Give the location of every WBC.
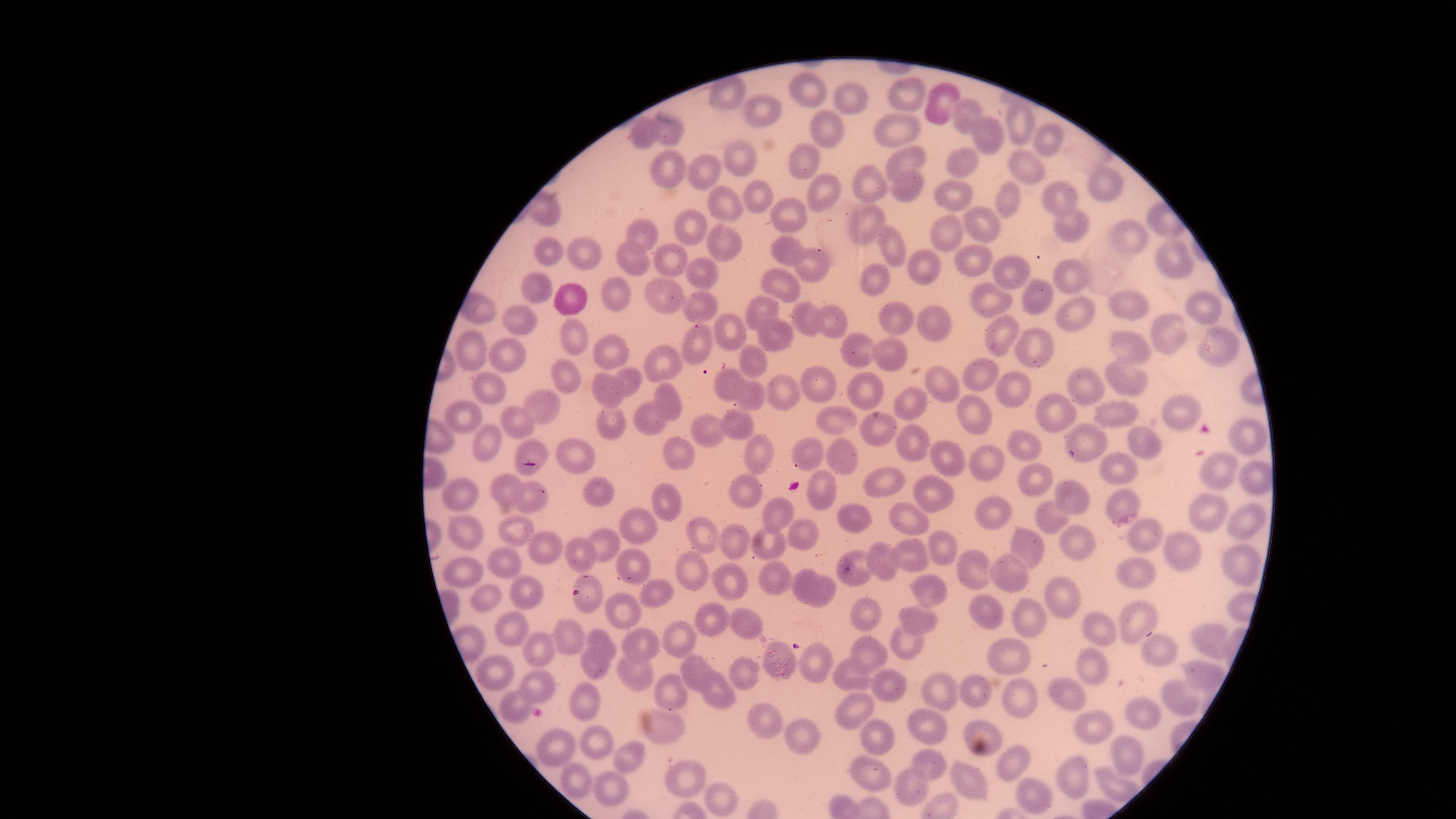
No WBCs identified.

Approximate marker points as {x, y} in pixels.
Summary:
  - Uninfected RBCs: {811, 80}, {914, 95}, {846, 96}, {942, 103}, {761, 109}, {966, 114}, {1020, 126}, {645, 127}, {825, 128}, {899, 128}, {670, 131}, {989, 135}, {1050, 141}, {742, 156}, {962, 159}, {802, 162}, {667, 165}, {903, 166}, {1026, 166}, {701, 174}, {863, 183}, {1100, 183}, {823, 190}, {753, 191}, {901, 192}, {951, 192}, {1014, 201}, {1060, 201}, {721, 202}, {787, 211}, {868, 215}, {1070, 223}, {988, 224}, {693, 226}, {1127, 232}, {646, 234}, {951, 234}, {726, 245}, {787, 247}, {896, 248}, {546, 250}, {588, 254}, {970, 255}, {804, 256}, {674, 258}, {635, 259}, {1167, 261}, {926, 262}, {696, 266}, {1008, 271}, {785, 276}, {880, 278}, {1065, 279}, {1032, 288}, {619, 291}, {664, 293}, {535, 295}, {987, 300}, {567, 301}, {704, 304}, {1203, 305}, {759, 307}, {1119, 308}, {1070, 311}, {834, 315}, {523, 316}, {929, 318}, {810, 320}, {898, 320}, {727, 329}, {995, 331}, {572, 333}, {773, 336}, {691, 339}, {1174, 339}, {1032, 341}, {612, 345}, {1129, 346}, {476, 347}, {856, 349}, {1219, 350}, {511, 354}, {884, 356}, {753, 359}, {663, 362}, {627, 374}, {566, 376}, {983, 377}, {1129, 378}, {821, 379}, {934, 381}, {484, 384}, {724, 386}, {608, 387}, {1084, 387}, {864, 390}, {1010, 392}, {777, 395}, {752, 396}, {671, 398}, {918, 399}, {544, 404}, {1056, 409}, {1177, 410}, {977, 411}, {828, 413}, {466, 415}, {1114, 416}, {649, 419}, {521, 420}, {611, 421}, {739, 421}, {879, 429}, {709, 430}, {1086, 436}, {913, 437}, {1244, 437}, {488, 443}, {1142, 443}, {1027, 446}, {525, 447}, {762, 451}, {574, 453}, {677, 453}, {811, 454}, {841, 456}, {946, 457}, {985, 459}, {1127, 467}, {1251, 468}, {1220, 469}, {1040, 476}, {888, 479}, {744, 486}, {597, 487}, {460, 489}, {507, 489}, {827, 492}, {932, 493}, {1070, 493}, {536, 495}, {668, 502}, {1124, 505}, {993, 507}, {776, 511}, {1213, 513}, {1043, 514}, {847, 517}, {910, 517}, {1243, 523}, {642, 524}, {462, 526}, {517, 527}, {799, 529}, {708, 534}, {1145, 537}, {606, 541}, {767, 541}, {1075, 541}, {540, 543}, {735, 546}, {933, 546}, {1025, 547}, {1183, 550}, {586, 552}, {886, 558}, {910, 558}, {1239, 559}, {505, 561}, {632, 565}, {1136, 567}, {694, 569}, {859, 570}, {975, 570}, {1009, 570}, {466, 573}, {775, 579}, {802, 580}, {729, 581}, {925, 589}, {825, 590}, {656, 591}, {1056, 592}, {521, 593}, {590, 597}, {490, 602}, {622, 603}, {869, 608}, {983, 610}, {714, 619}, {747, 619}, {1022, 620}, {1139, 620}, {918, 623}, {565, 629}, {1103, 629}, {508, 630}, {677, 632}, {1207, 635}, {598, 637}, {904, 639}, {644, 641}, {1154, 651}, {873, 652}, {775, 655}, {545, 657}, {1014, 657}, {814, 660}, {594, 667}, {1090, 667}, {692, 669}, {494, 670}, {748, 671}, {849, 671}, {632, 673}, {1197, 673}, {938, 681}, {542, 686}, {672, 686}, {888, 686}, {979, 690}, {719, 694}, {1068, 694}, {583, 697}, {1177, 697}, {1019, 699}, {521, 704}, {851, 708}, {1143, 712}, {762, 721}, {1093, 728}, {668, 732}, {924, 732}, {981, 732}, {596, 736}, {871, 737}, {799, 738}, {562, 744}, {1122, 745}, {627, 756}, {934, 762}, {1016, 763}, {869, 769}, {1082, 772}, {965, 781}, {686, 782}, {909, 783}, {577, 786}, {614, 791}, {720, 795}, {1027, 797}
  - Preparation: thin blood film
  - Capture: smartphone photograph through the microscope eyepiece
  - Visible region: circular
  - Image size: 1456×819 pixels
  - Field of view: single
  - Presence: no malaria parasites detected
  - Stain: Giemsa